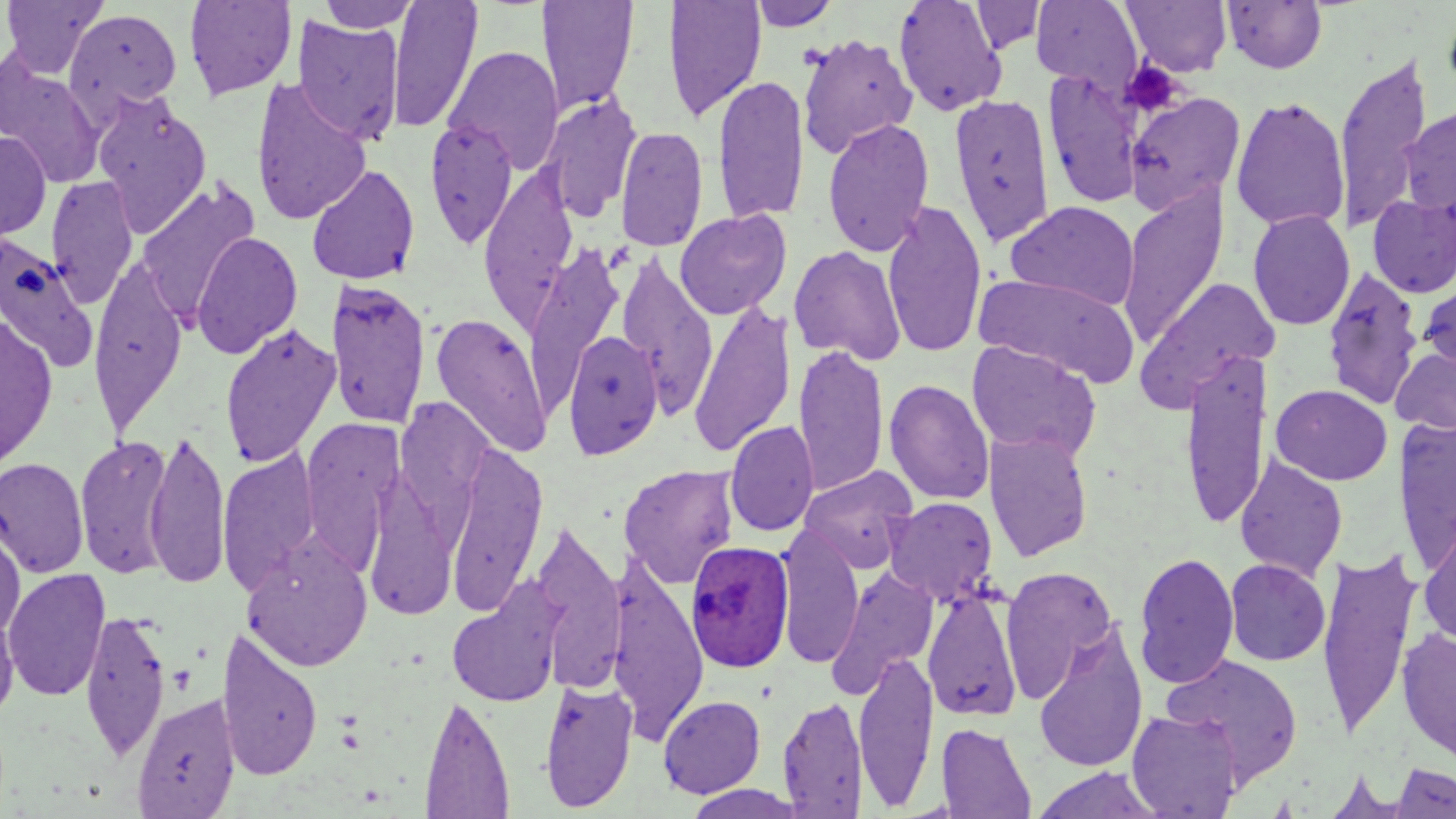

slide_level_diagnosis: Plasmodium ovale
stain: May-Grünwald-Giemsa
plasmodium_ovale_infected_red_blood_cell_locations: 'approximate bounding boxes as named x1/y1/x2/y2 corners in pixels: (x1=686, y1=538, x2=794, y2=673)'
preparation: thin blood film
image_size: 1456×819 pixels
magnification: 1000x
field_of_view: one of a larger specimen
uninfected_red_blood_cell_locations: 'approximate bounding boxes as named x1/y1/x2/y2 corners in pixels: (x1=1, y1=0, x2=107, y2=78), (x1=183, y1=0, x2=297, y2=100), (x1=386, y1=0, x2=482, y2=132), (x1=663, y1=0, x2=766, y2=122), (x1=893, y1=0, x2=1008, y2=116), (x1=1121, y1=0, x2=1232, y2=76), (x1=318, y1=1, x2=419, y2=33), (x1=538, y1=1, x2=639, y2=116), (x1=747, y1=1, x2=840, y2=31), (x1=970, y1=1, x2=1047, y2=55), (x1=1031, y1=1, x2=1144, y2=92), (x1=1222, y1=1, x2=1328, y2=74), (x1=1442, y1=3, x2=1456, y2=103), (x1=64, y1=8, x2=183, y2=118), (x1=292, y1=16, x2=405, y2=144), (x1=797, y1=33, x2=917, y2=158), (x1=444, y1=45, x2=565, y2=173), (x1=1332, y1=53, x2=1434, y2=232), (x1=0, y1=54, x2=105, y2=187), (x1=1043, y1=70, x2=1145, y2=209), (x1=712, y1=74, x2=809, y2=225), (x1=250, y1=77, x2=373, y2=225), (x1=92, y1=92, x2=211, y2=235), (x1=949, y1=92, x2=1056, y2=246), (x1=1125, y1=92, x2=1245, y2=214), (x1=539, y1=93, x2=642, y2=222), (x1=1231, y1=95, x2=1349, y2=233), (x1=1399, y1=104, x2=1456, y2=220), (x1=821, y1=117, x2=935, y2=257), (x1=424, y1=118, x2=519, y2=249), (x1=615, y1=125, x2=708, y2=253), (x1=0, y1=131, x2=51, y2=241), (x1=478, y1=163, x2=579, y2=333), (x1=306, y1=164, x2=421, y2=285), (x1=45, y1=175, x2=139, y2=307), (x1=136, y1=180, x2=260, y2=324), (x1=1116, y1=184, x2=1229, y2=350), (x1=1367, y1=194, x2=1456, y2=298), (x1=882, y1=199, x2=988, y2=358), (x1=1005, y1=200, x2=1139, y2=311), (x1=675, y1=208, x2=792, y2=320), (x1=1247, y1=209, x2=1355, y2=331), (x1=191, y1=231, x2=302, y2=359), (x1=0, y1=233, x2=99, y2=375), (x1=523, y1=245, x2=625, y2=412), (x1=789, y1=245, x2=906, y2=365), (x1=616, y1=252, x2=718, y2=416), (x1=88, y1=260, x2=188, y2=434), (x1=1322, y1=265, x2=1424, y2=411), (x1=975, y1=272, x2=1141, y2=385), (x1=1137, y1=277, x2=1281, y2=409), (x1=325, y1=278, x2=432, y2=430), (x1=1419, y1=278, x2=1456, y2=379), (x1=688, y1=300, x2=797, y2=458), (x1=430, y1=311, x2=553, y2=458), (x1=0, y1=314, x2=58, y2=470), (x1=219, y1=322, x2=341, y2=468), (x1=561, y1=329, x2=665, y2=459), (x1=967, y1=342, x2=1101, y2=461), (x1=793, y1=345, x2=889, y2=497), (x1=1391, y1=345, x2=1456, y2=436), (x1=1179, y1=350, x2=1271, y2=531), (x1=884, y1=378, x2=995, y2=505), (x1=1271, y1=384, x2=1393, y2=486), (x1=1394, y1=418, x2=1456, y2=574), (x1=301, y1=420, x2=403, y2=576), (x1=724, y1=420, x2=819, y2=537), (x1=984, y1=428, x2=1094, y2=562), (x1=144, y1=430, x2=231, y2=589), (x1=75, y1=434, x2=175, y2=580), (x1=445, y1=441, x2=549, y2=614), (x1=218, y1=450, x2=320, y2=593), (x1=1234, y1=454, x2=1348, y2=582), (x1=0, y1=457, x2=89, y2=578), (x1=619, y1=464, x2=739, y2=589), (x1=799, y1=466, x2=918, y2=575), (x1=362, y1=474, x2=460, y2=623), (x1=884, y1=496, x2=998, y2=606), (x1=1418, y1=518, x2=1456, y2=650), (x1=529, y1=521, x2=627, y2=691), (x1=0, y1=525, x2=25, y2=639), (x1=775, y1=525, x2=863, y2=670), (x1=242, y1=538, x2=373, y2=672), (x1=1316, y1=548, x2=1421, y2=739), (x1=1133, y1=551, x2=1239, y2=689), (x1=1225, y1=558, x2=1330, y2=666), (x1=607, y1=563, x2=710, y2=741), (x1=999, y1=565, x2=1118, y2=703), (x1=827, y1=566, x2=939, y2=696), (x1=3, y1=568, x2=111, y2=702), (x1=446, y1=580, x2=566, y2=709), (x1=923, y1=586, x2=1022, y2=722), (x1=0, y1=602, x2=19, y2=723), (x1=79, y1=607, x2=171, y2=764), (x1=1032, y1=623, x2=1148, y2=773), (x1=216, y1=627, x2=324, y2=781), (x1=1397, y1=628, x2=1456, y2=764), (x1=853, y1=649, x2=939, y2=810), (x1=1162, y1=654, x2=1304, y2=787), (x1=539, y1=678, x2=638, y2=813), (x1=132, y1=693, x2=240, y2=818), (x1=419, y1=693, x2=515, y2=818), (x1=658, y1=695, x2=766, y2=798), (x1=777, y1=695, x2=868, y2=817), (x1=1126, y1=708, x2=1244, y2=818), (x1=937, y1=723, x2=1036, y2=818), (x1=1387, y1=762, x2=1456, y2=818), (x1=1030, y1=767, x2=1163, y2=819)'
modality: light microscopy
platelet_locations: 'approximate bounding boxes as named x1/y1/x2/y2 corners in pixels: (x1=1120, y1=61, x2=1184, y2=117)'